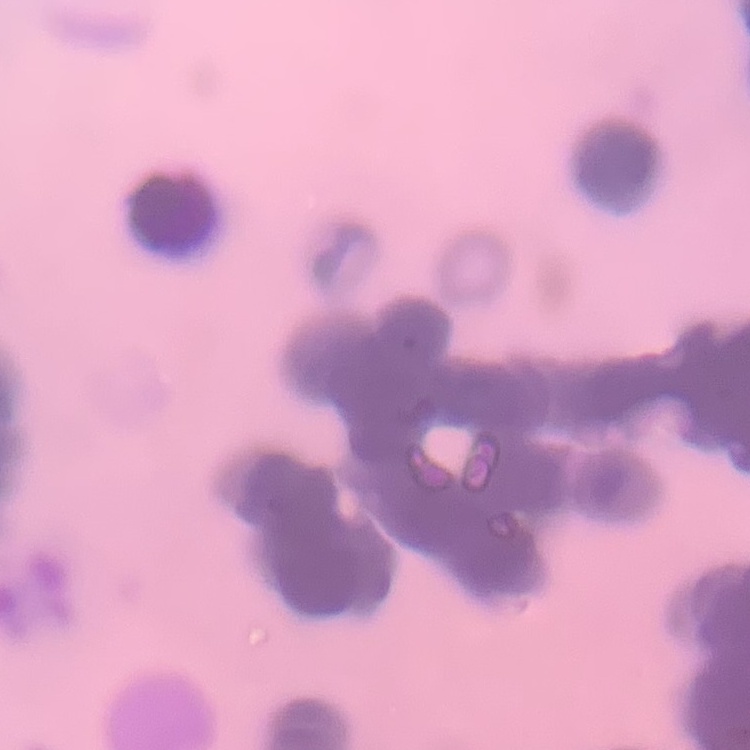

erythrocyte morphology = rouleaux formation
preparation = thin blood smear
image type = one tile cut from a larger photomicrograph
stain = Field's or Giemsa